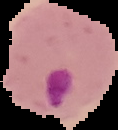

preparation = thin blood film
malaria status = parasitized
image size = 118×130 pixels
image type = cell region segmented out of the field of view; surrounding area masked to black